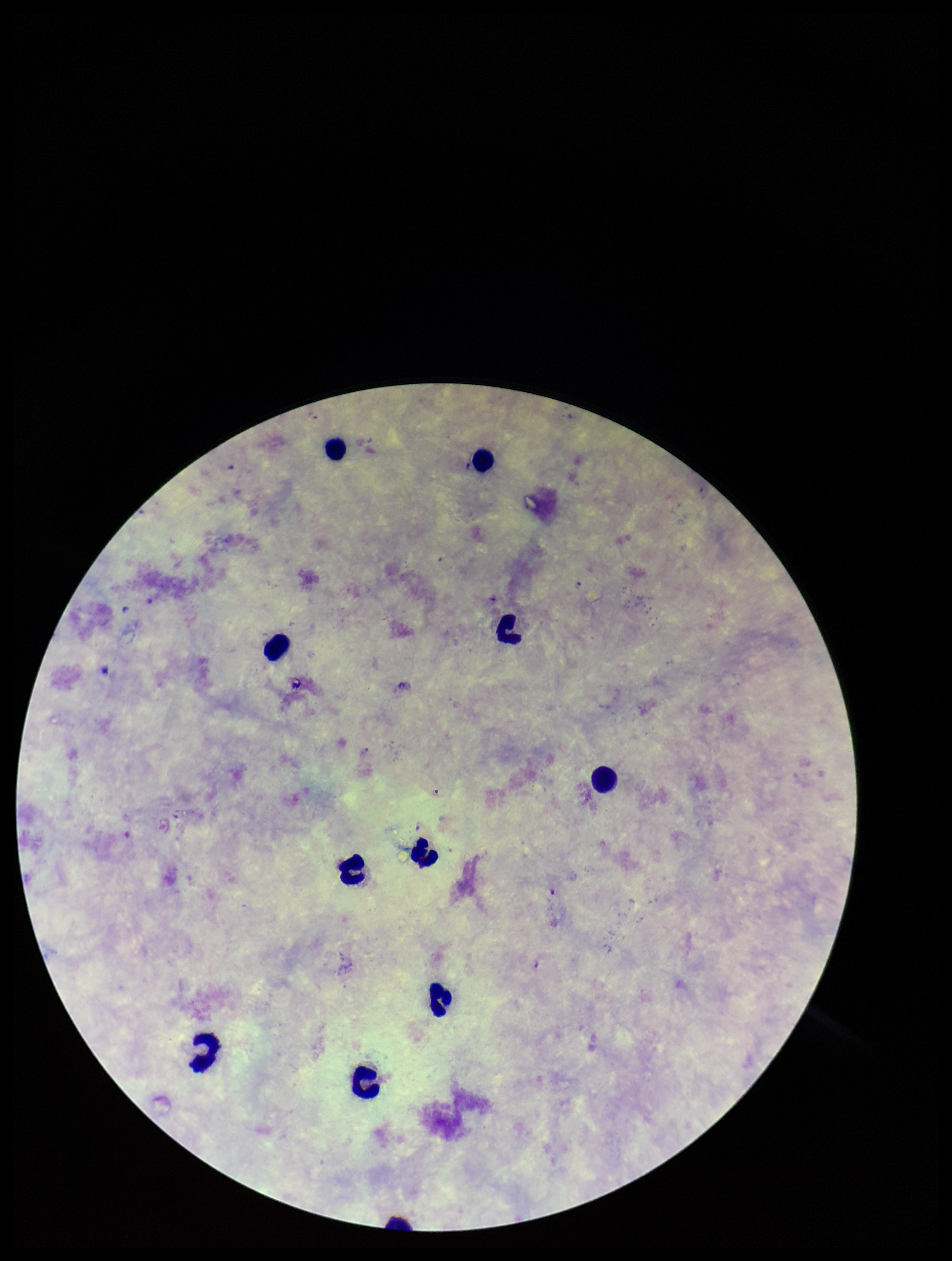
Species reported for this patient: Plasmodium falciparum. Image is 952×1261 pixels. Patient malaria status: infected. One field from this slide. Preparation: thick. Parasite count: 0. Plasmodium parasites: none detected. Giemsa stain. Smartphone photograph taken through the eyepiece of a microscope. Leukocyte count: 10.